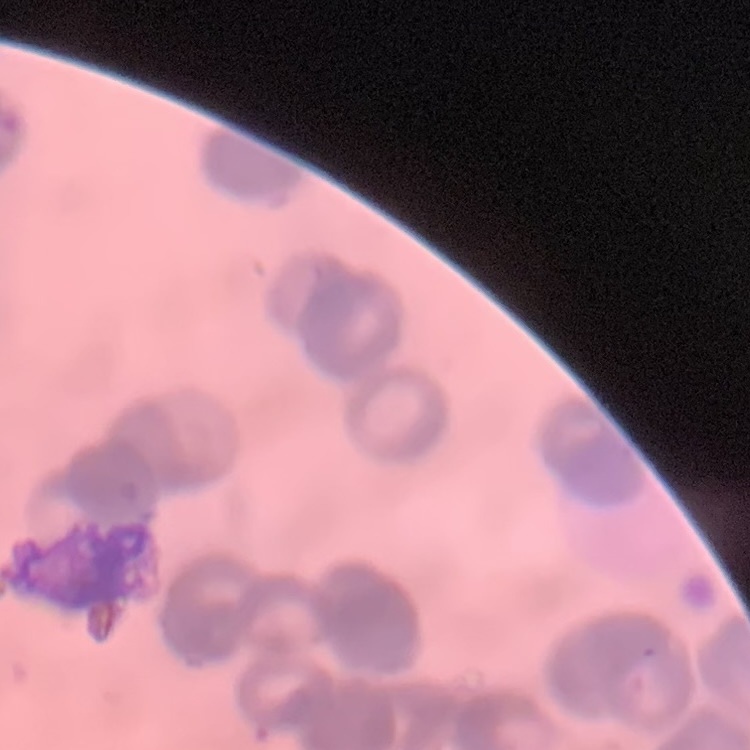
Summary:
  - Erythrocyte morphology: rouleaux formation
  - Stain: Field's or Giemsa
  - Preparation: thin peripheral smear
  - Image type: square crop of a larger photomicrograph